Draw a bounding box around every parasitised red blood cell, every trophozoite, every gametocyte, every leukocyte, and every artifact (platelet-like body, stain precipitate, or debris).
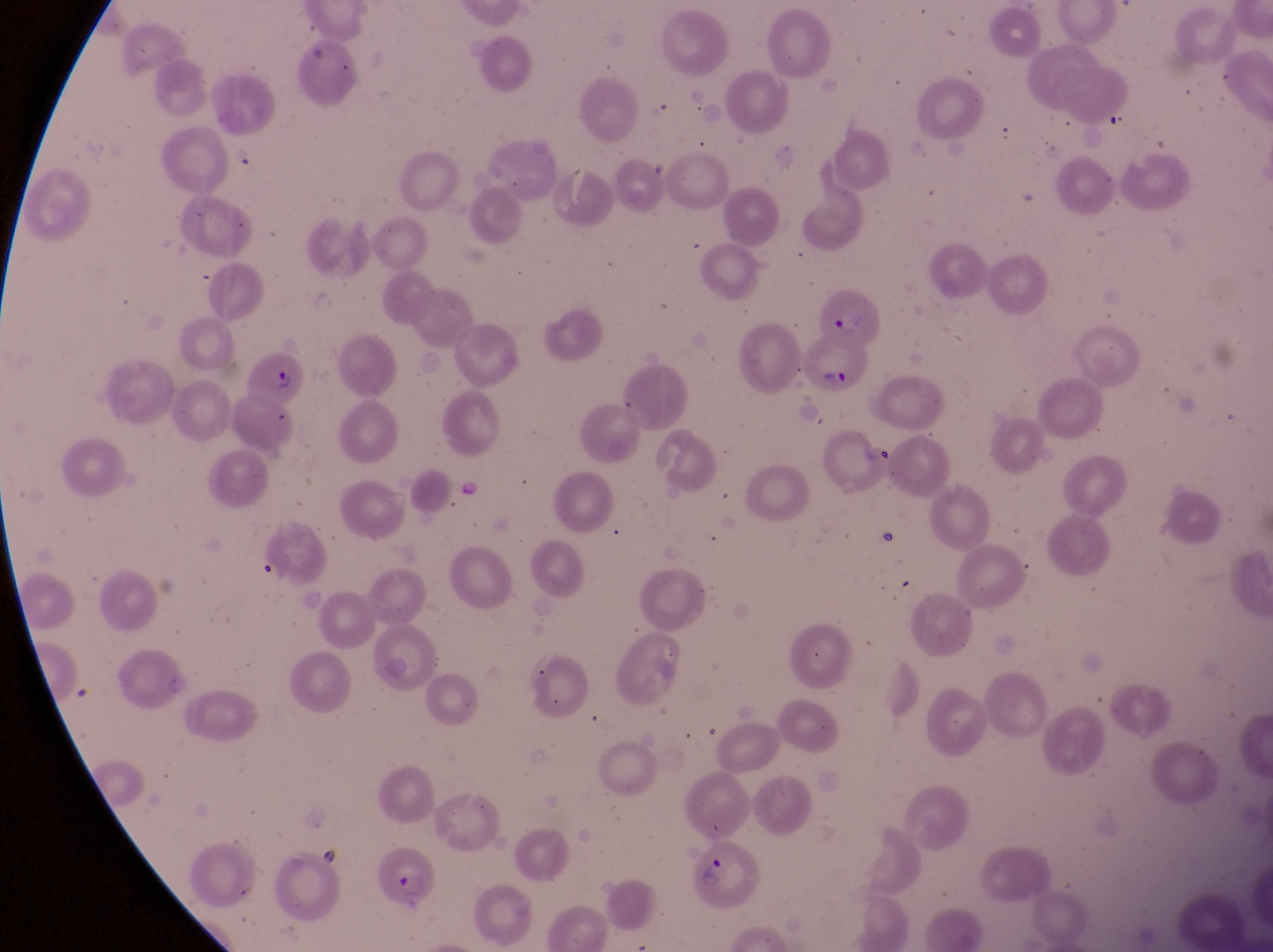
Approximate bounding boxes as (left, top, right, bottom) in pixels.
Parasitised red blood cells: (817, 289, 889, 346), (804, 340, 873, 397), (239, 357, 314, 409), (684, 847, 764, 909), (369, 854, 444, 907).
No leukocytes observed.

Summary:
  - Capture: smartphone photograph through the eyepiece of an Olympus CX-23 microscope
  - Country: Uganda
  - Image size: 1273×952 pixels
  - Field of view: single
  - Preparation: thin blood film
  - Magnification: 1000x